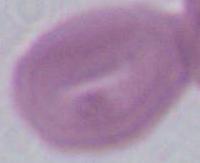
An erythrocyte is seen. Captured at 1000x magnification. Micrograph.